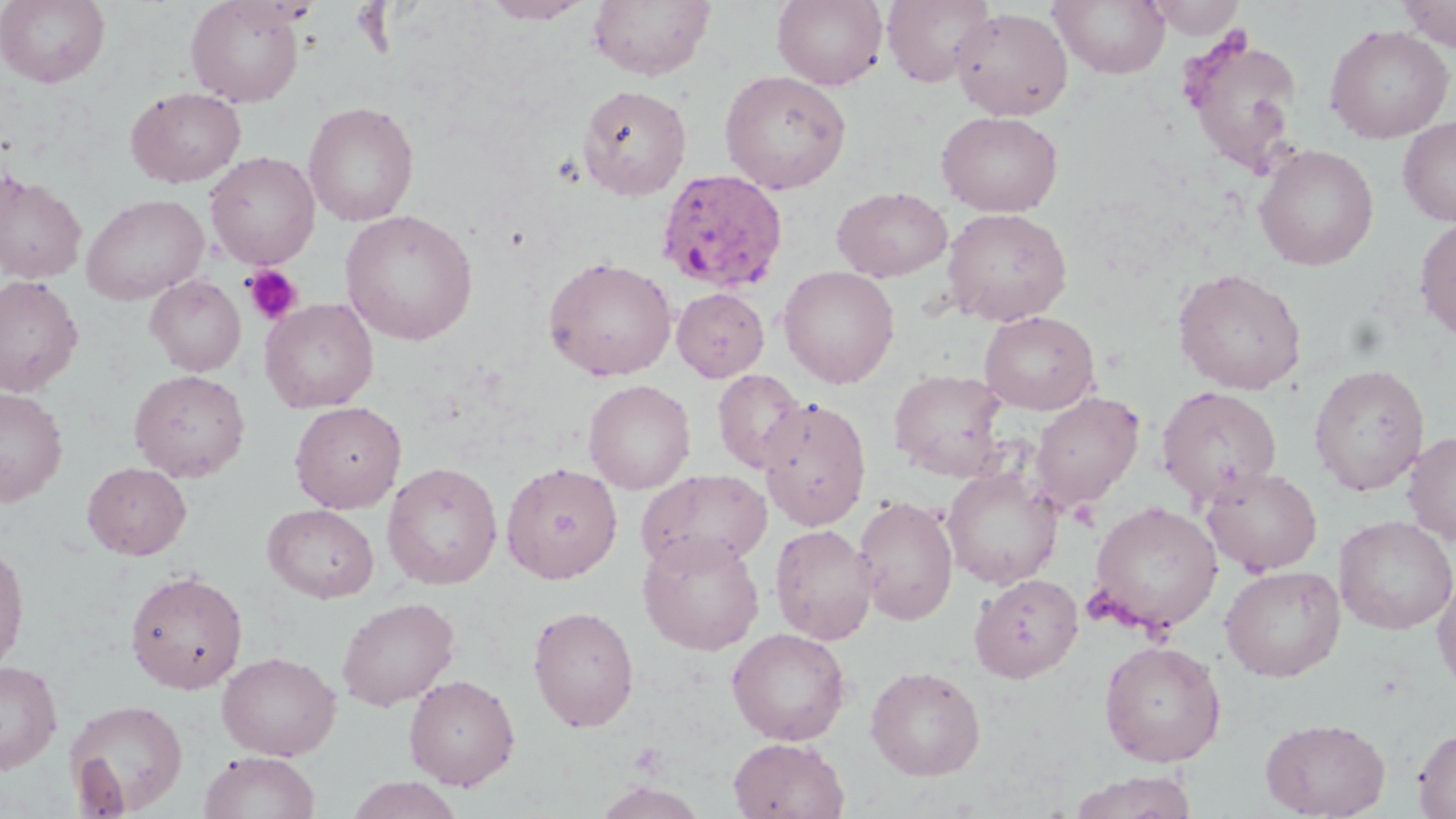

slide_level_diagnosis: Plasmodium ovale
field_of_view: single
preparation: thin blood smear
modality: optical microscopy
platelet_locations: 'approximate bounding boxes as named x1/y1/x2/y2 corners in pixels: (x1=242, y1=265, x2=303, y2=326)'
stain: May-Grünwald-Giemsa
image_size: 1456×819 pixels
uninfected_red_blood_cell_locations: 'approximate bounding boxes as named x1/y1/x2/y2 corners in pixels: (x1=0, y1=0, x2=110, y2=88), (x1=186, y1=0, x2=305, y2=106), (x1=481, y1=0, x2=593, y2=24), (x1=588, y1=0, x2=715, y2=81), (x1=772, y1=0, x2=888, y2=90), (x1=882, y1=0, x2=995, y2=87), (x1=1050, y1=0, x2=1170, y2=79), (x1=1143, y1=0, x2=1247, y2=39), (x1=1396, y1=0, x2=1456, y2=51), (x1=951, y1=7, x2=1073, y2=121), (x1=1325, y1=24, x2=1454, y2=143), (x1=1181, y1=33, x2=1305, y2=178), (x1=719, y1=70, x2=851, y2=194), (x1=577, y1=84, x2=692, y2=200), (x1=125, y1=87, x2=247, y2=188), (x1=303, y1=101, x2=419, y2=227), (x1=936, y1=111, x2=1063, y2=216), (x1=1398, y1=116, x2=1456, y2=227), (x1=1254, y1=144, x2=1379, y2=270), (x1=205, y1=152, x2=320, y2=269), (x1=0, y1=170, x2=87, y2=284), (x1=832, y1=186, x2=952, y2=282), (x1=81, y1=193, x2=208, y2=304), (x1=941, y1=208, x2=1072, y2=326), (x1=340, y1=209, x2=478, y2=345), (x1=1415, y1=217, x2=1456, y2=341), (x1=544, y1=256, x2=677, y2=381), (x1=778, y1=265, x2=900, y2=388), (x1=1173, y1=268, x2=1307, y2=394), (x1=0, y1=275, x2=83, y2=397), (x1=146, y1=275, x2=246, y2=376), (x1=672, y1=287, x2=769, y2=382), (x1=260, y1=298, x2=378, y2=413), (x1=979, y1=310, x2=1100, y2=414), (x1=1309, y1=364, x2=1430, y2=496), (x1=128, y1=369, x2=250, y2=483), (x1=712, y1=369, x2=807, y2=474), (x1=888, y1=369, x2=1010, y2=481), (x1=584, y1=379, x2=696, y2=494), (x1=1156, y1=385, x2=1283, y2=506), (x1=0, y1=387, x2=68, y2=505), (x1=1029, y1=392, x2=1144, y2=513), (x1=757, y1=396, x2=871, y2=529), (x1=290, y1=401, x2=407, y2=513), (x1=1402, y1=430, x2=1456, y2=545), (x1=382, y1=461, x2=503, y2=590), (x1=82, y1=462, x2=192, y2=560), (x1=501, y1=462, x2=623, y2=582), (x1=941, y1=465, x2=1063, y2=590), (x1=1201, y1=466, x2=1323, y2=575), (x1=636, y1=468, x2=773, y2=575), (x1=853, y1=495, x2=958, y2=625), (x1=1089, y1=501, x2=1223, y2=634), (x1=263, y1=503, x2=379, y2=602), (x1=1334, y1=516, x2=1456, y2=635), (x1=770, y1=523, x2=877, y2=645), (x1=638, y1=532, x2=765, y2=655), (x1=0, y1=541, x2=30, y2=676), (x1=1220, y1=565, x2=1346, y2=681), (x1=124, y1=570, x2=249, y2=694), (x1=1433, y1=570, x2=1456, y2=695), (x1=970, y1=573, x2=1083, y2=683), (x1=336, y1=596, x2=459, y2=710), (x1=527, y1=605, x2=639, y2=731), (x1=727, y1=627, x2=852, y2=745), (x1=1098, y1=639, x2=1227, y2=767), (x1=217, y1=651, x2=341, y2=761), (x1=0, y1=660, x2=63, y2=774), (x1=865, y1=665, x2=985, y2=780), (x1=403, y1=674, x2=520, y2=790), (x1=64, y1=698, x2=188, y2=816), (x1=1261, y1=717, x2=1390, y2=818), (x1=1413, y1=727, x2=1456, y2=818), (x1=728, y1=737, x2=850, y2=819), (x1=198, y1=751, x2=321, y2=819), (x1=1069, y1=771, x2=1197, y2=819), (x1=344, y1=776, x2=465, y2=819), (x1=594, y1=780, x2=708, y2=819)'
magnification: 1000x
plasmodium_ovale_infected_red_blood_cell_locations: 'approximate bounding boxes as named x1/y1/x2/y2 corners in pixels: (x1=657, y1=167, x2=788, y2=292)'